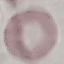

result: no malaria parasites detected
stain: Giemsa
image_type: automatically extracted cell patch, resized to 64 × 64 pixels
capture: smartphone through the microscope eyepiece
preparation: thin smear